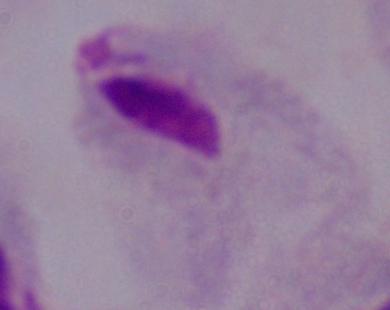

{
  "magnification": "1000x",
  "modality": "micrograph",
  "identification": "trichomonad"
}